Identify the blood parasite species.
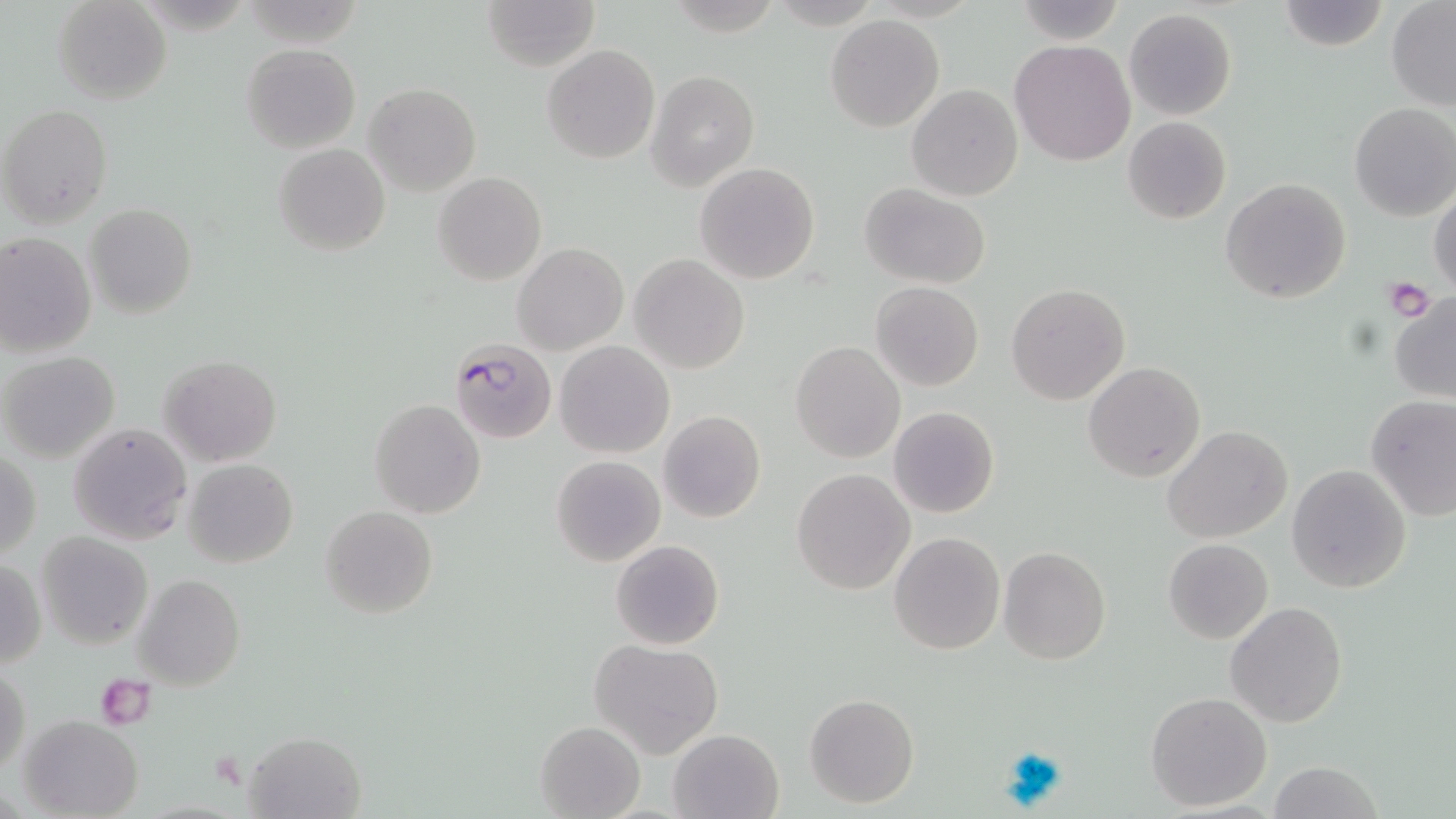

Plasmodium falciparum.

uninfected red blood cell locations = approximate bounding boxes as named x1/y1/x2/y2 corners in pixels: (x1=53, y1=0, x2=172, y2=105), (x1=480, y1=0, x2=598, y2=71), (x1=1275, y1=0, x2=1388, y2=51), (x1=1015, y1=1, x2=1127, y2=45), (x1=1386, y1=2, x2=1456, y2=110), (x1=1124, y1=8, x2=1237, y2=121), (x1=825, y1=14, x2=944, y2=132), (x1=1010, y1=40, x2=1136, y2=167), (x1=241, y1=43, x2=361, y2=153), (x1=542, y1=44, x2=660, y2=164), (x1=646, y1=70, x2=759, y2=190), (x1=364, y1=83, x2=481, y2=197), (x1=907, y1=84, x2=1024, y2=201), (x1=1349, y1=102, x2=1456, y2=221), (x1=1, y1=104, x2=114, y2=229), (x1=1122, y1=116, x2=1232, y2=225), (x1=273, y1=143, x2=390, y2=256), (x1=695, y1=162, x2=820, y2=284), (x1=433, y1=172, x2=547, y2=285), (x1=1220, y1=178, x2=1350, y2=303), (x1=860, y1=183, x2=991, y2=288), (x1=1430, y1=184, x2=1455, y2=297), (x1=84, y1=202, x2=197, y2=319), (x1=0, y1=231, x2=97, y2=358), (x1=513, y1=242, x2=628, y2=354), (x1=629, y1=254, x2=750, y2=373), (x1=871, y1=282, x2=983, y2=391), (x1=1006, y1=282, x2=1130, y2=404), (x1=1389, y1=292, x2=1456, y2=404), (x1=555, y1=339, x2=674, y2=458), (x1=791, y1=341, x2=904, y2=463), (x1=0, y1=352, x2=121, y2=464), (x1=161, y1=354, x2=281, y2=466), (x1=1083, y1=361, x2=1205, y2=483), (x1=1365, y1=395, x2=1455, y2=520), (x1=369, y1=399, x2=486, y2=518), (x1=888, y1=405, x2=999, y2=518), (x1=658, y1=410, x2=765, y2=523), (x1=67, y1=422, x2=193, y2=545), (x1=1162, y1=425, x2=1294, y2=545), (x1=1, y1=449, x2=42, y2=560), (x1=551, y1=455, x2=666, y2=566), (x1=183, y1=459, x2=299, y2=569), (x1=1287, y1=463, x2=1411, y2=592), (x1=791, y1=468, x2=915, y2=595), (x1=320, y1=505, x2=438, y2=618), (x1=35, y1=530, x2=153, y2=650), (x1=888, y1=532, x2=1005, y2=654), (x1=610, y1=539, x2=725, y2=650), (x1=1163, y1=539, x2=1273, y2=644), (x1=997, y1=545, x2=1110, y2=666), (x1=1, y1=558, x2=46, y2=671), (x1=133, y1=575, x2=245, y2=691), (x1=1224, y1=602, x2=1348, y2=729), (x1=589, y1=639, x2=724, y2=758), (x1=1, y1=667, x2=30, y2=776), (x1=1144, y1=691, x2=1273, y2=810), (x1=805, y1=693, x2=919, y2=808), (x1=19, y1=715, x2=144, y2=818), (x1=534, y1=720, x2=646, y2=818), (x1=667, y1=728, x2=785, y2=818), (x1=243, y1=729, x2=365, y2=818), (x1=1267, y1=759, x2=1383, y2=819)
modality = light microscopy
stain = May-Grünwald-Giemsa
preparation = thin blood smear
Plasmodium falciparum-infected red blood cell locations = approximate bounding boxes as named x1/y1/x2/y2 corners in pixels: (x1=449, y1=339, x2=558, y2=443)
magnification = 1000x
field of view = one of a larger specimen
platelet locations = approximate bounding boxes as named x1/y1/x2/y2 corners in pixels: (x1=1383, y1=276, x2=1433, y2=320), (x1=94, y1=671, x2=153, y2=727)
image size = 1456×819 pixels